Give the position of every leukocyte visible.
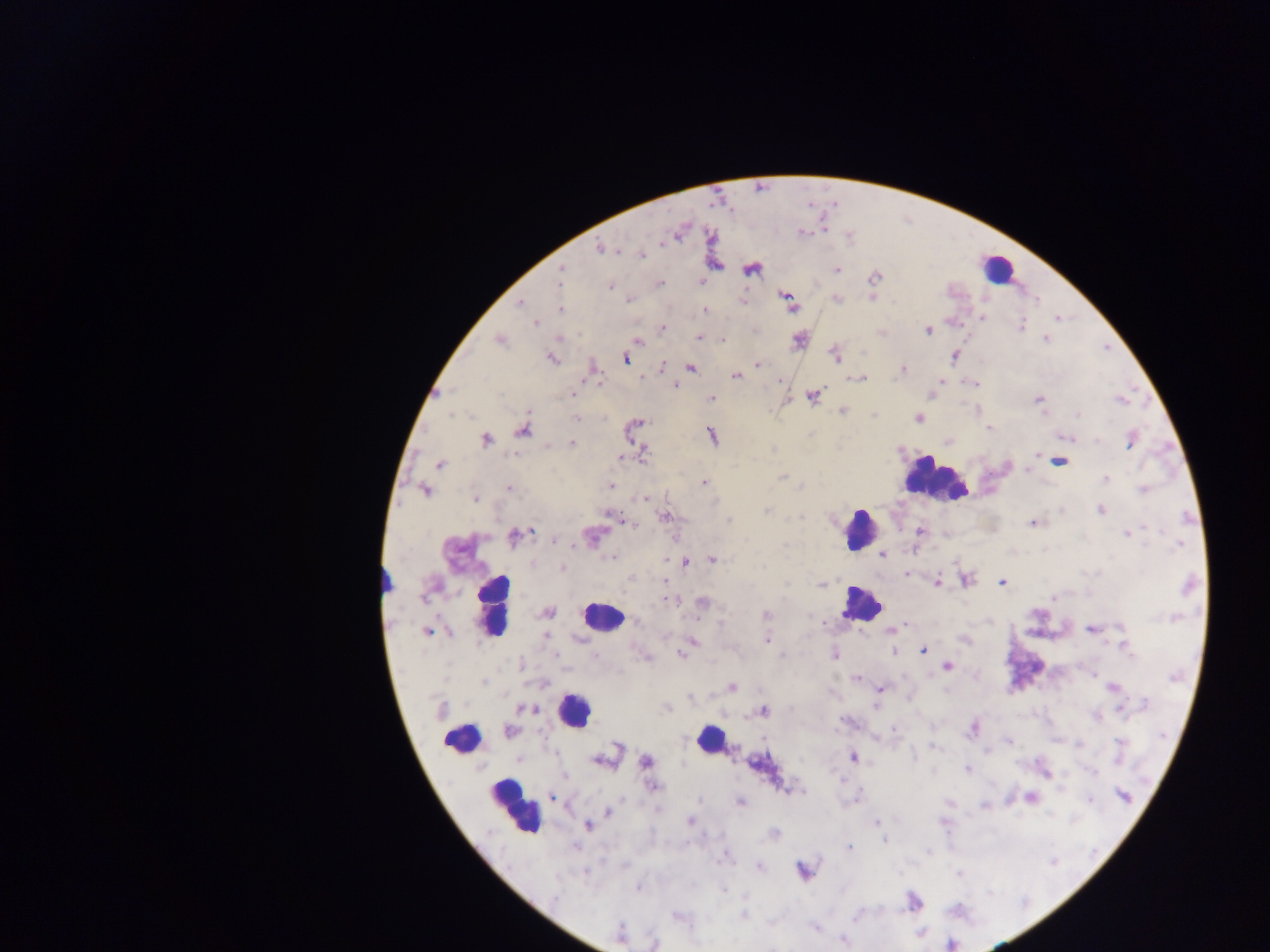

Approximate centers as x y in pixels.
Leukocytes: 996 267; 934 480; 859 529; 860 603; 493 609; 603 617; 574 711; 459 739; 709 739; 514 807.

Summary:
  - Plasmodium parasite locations: 802 232; 599 248; 641 255; 837 269; 561 270; 752 270; 874 277; 659 284; 610 286; 629 300; 837 300; 743 301; 520 302; 788 302; 560 309; 705 311; 982 317; 1057 318; 535 324; 1021 325; 662 327; 928 331; 699 337; 722 339; 1045 339; 499 341; 638 341; 799 341; 835 356; 955 356; 552 358; 626 358; 758 364; 661 367; 593 369; 691 369; 902 369; 736 376; 858 379; 941 381; 973 383; 675 385; 573 394; 813 396; 711 398; 1038 399; 1120 399; 842 411; 1078 415; 576 418; 918 418; 638 422; 990 428; 523 431; 712 436; 1067 437; 486 440; 1131 440; 1096 441; 572 443; 643 454; 1037 454; 1060 462; 441 464; 1027 472; 782 476; 1106 478; 704 482; 611 485; 802 486; 510 489; 425 490; 1142 490; 643 498; 475 499; 766 510; 1100 510; 610 516; 666 516; 729 521; 632 524; 1033 524; 920 532; 1127 534; 515 536; 591 536; 554 540; 1178 545; 883 555; 610 557; 712 560; 686 562; 563 568; 907 573; 631 579; 665 580; 965 580; 938 582; 1002 582; 821 585; 668 600; 702 603; 547 612; 767 615; 1173 618; 893 629; 1092 629; 1121 630; 427 632; 546 636; 767 640; 964 640; 693 644; 1127 648; 923 650; 894 651; 681 653; 834 655; 782 656; 645 657; 949 666; 856 679; 483 683; 732 687; 1113 688; 880 689; 1145 703; 876 706; 531 708; 667 708; 1123 709; 763 712; 1096 716; 894 729; 972 729; 509 731; 1008 741; 1120 744; 932 746; 854 758; 603 760; 647 762; 755 764; 967 769; 1092 772; 653 787; 1123 795; 551 796; 1031 797; 854 800; 1089 800; 740 801; 608 812; 690 822; 877 822; 589 826; 773 833; 884 840; 849 848; 725 857; 759 866; 803 871; 585 872; 959 874; 637 888; 723 889; 556 896; 744 915; 857 915; 677 917; 815 928; 620 933; 843 940; 655 943
  - Field of view: single
  - Country: Ghana
  - Capture: mobile-phone photograph through a microscope
  - Image size: 1270×952 pixels
  - Preparation: thick blood film